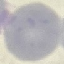

Malaria status: uninfected. Automatically extracted cell patch, resized to 64 × 64 pixels. Acquired by smartphone through the microscope eyepiece. Giemsa stain. Thin blood film.